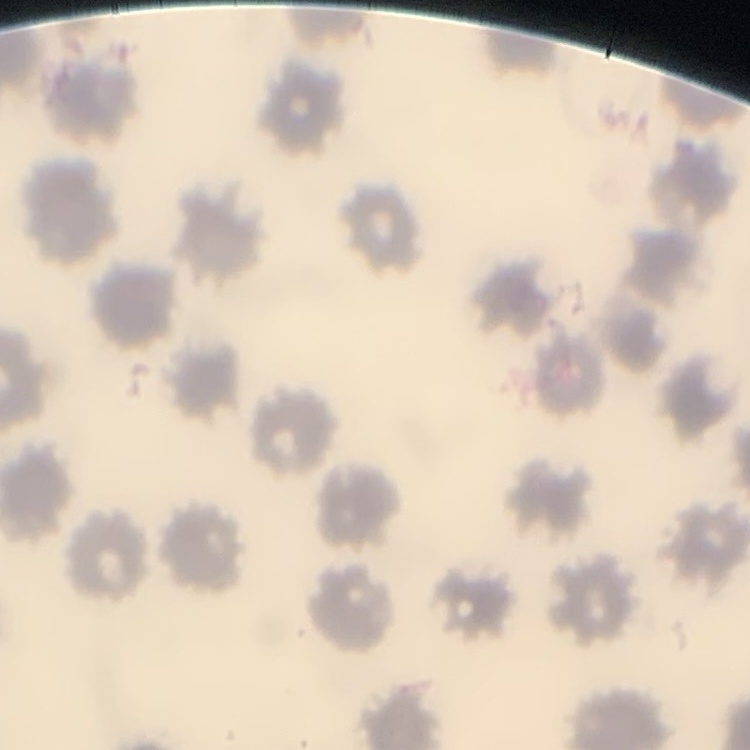

The red blood cells exhibit no rouleaux formation. Field's or Giemsa stain. One tile cut from a larger photomicrograph. Thin peripheral smear.